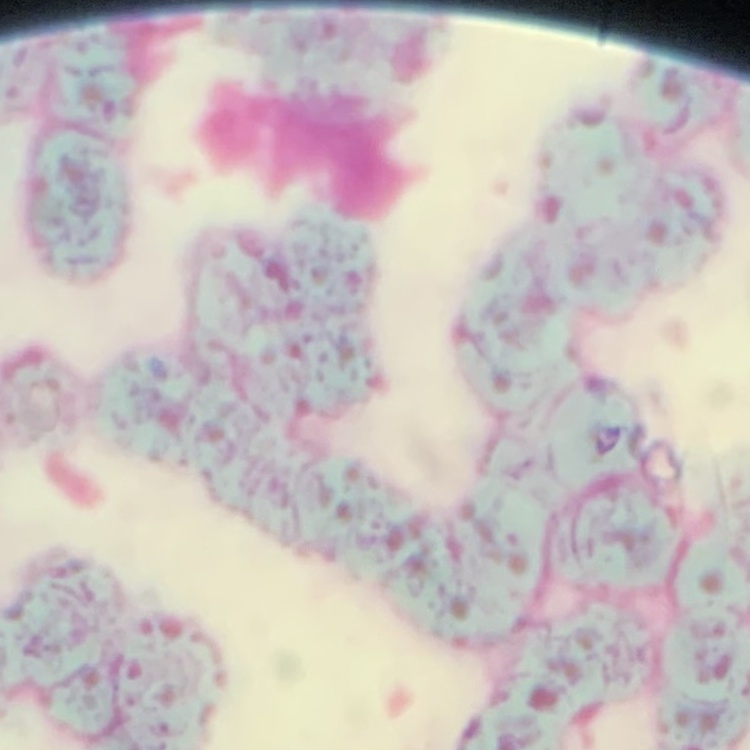

{
  "red_blood_cell_morphology": "rouleaux formation",
  "stain": "Field's or Giemsa",
  "image_type": "one tile cut from a larger photomicrograph",
  "preparation": "thin blood smear"
}